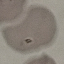
malaria status = uninfected
image type = automatically extracted cell patch, resized to 64 × 64 pixels
preparation = thin smear
capture = smartphone camera at the microscope eyepiece
stain = Giemsa